Assess for malaria.
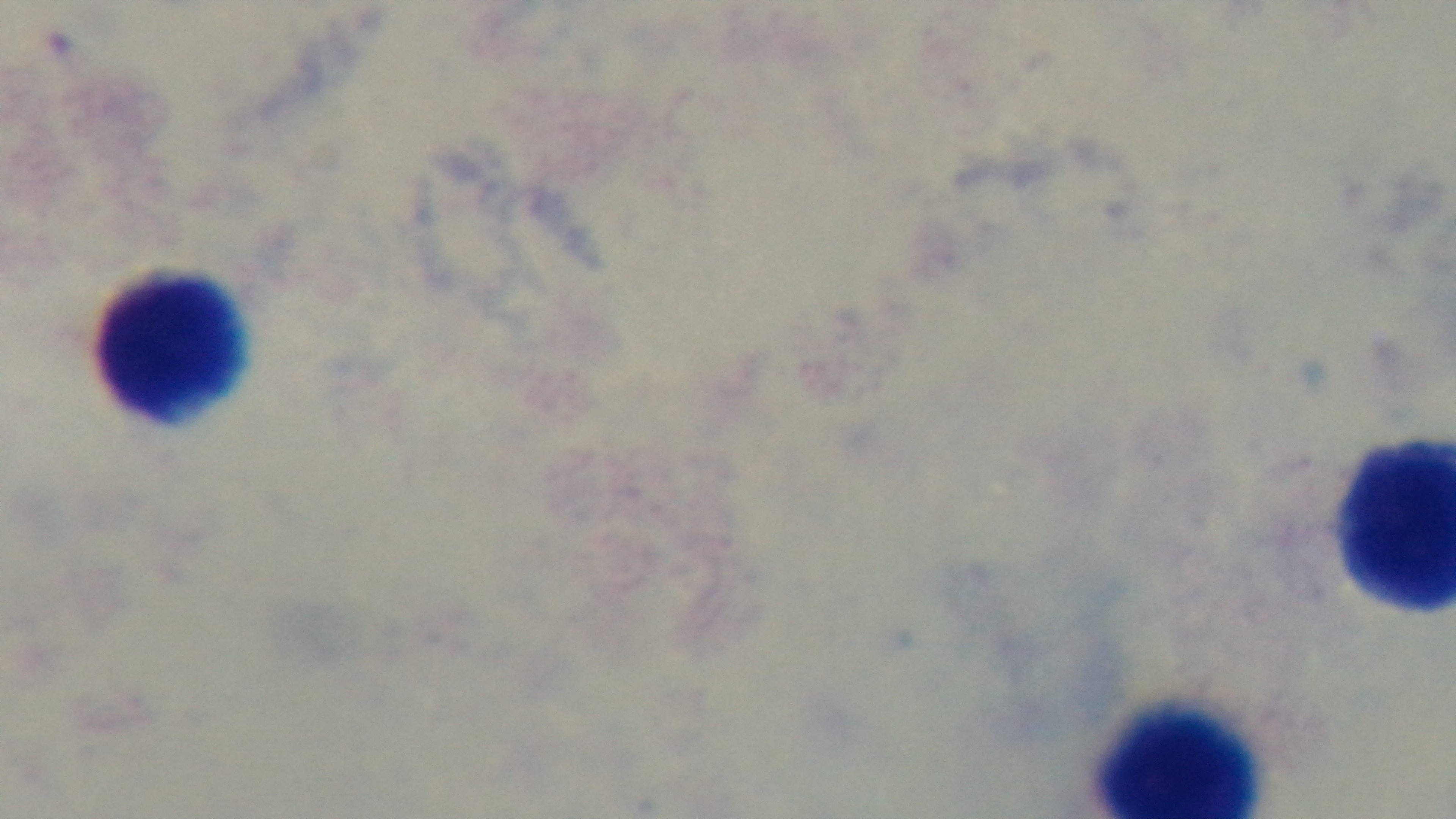

Uninfected.

Summary:
  - Preparation: thick smear
  - Stain: Giemsa
  - Capture: mounted 4K digital camera
  - Field of view: single
  - Objective: 100x oil immersion
  - Modality: light microscopy